Give the preparation type.
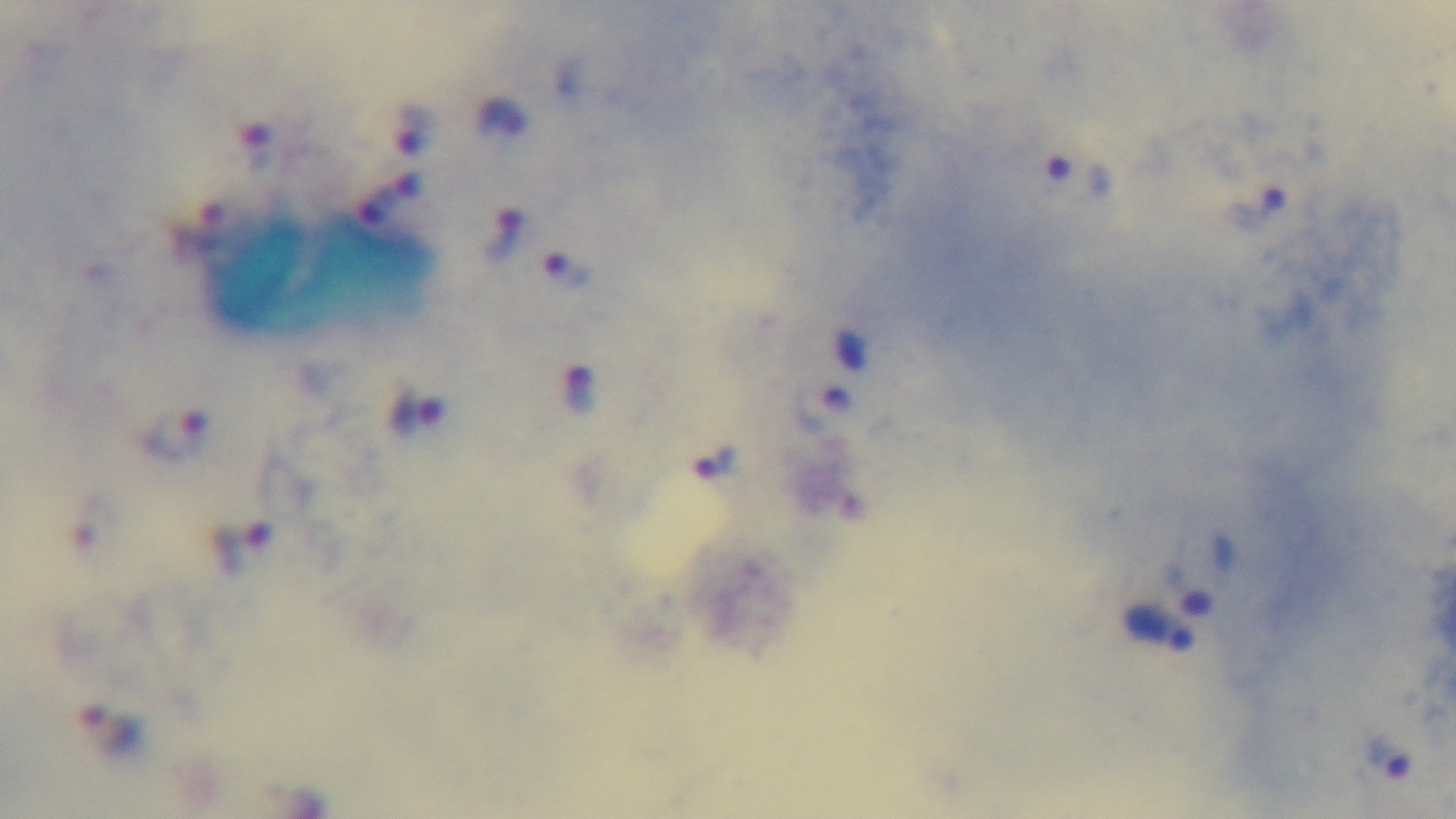

A thick smear.

objective: 100x oil immersion
stain: Giemsa
capture: mounted 4K digital camera
malaria_status: positive
field_of_view: single
modality: light microscopy